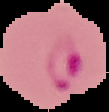
{
  "result": "malaria parasites detected",
  "image_size": "109×112 pixels",
  "preparation": "thin blood smear",
  "image_type": "segmented cell region with the area outside set to black"
}